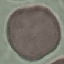
Result: no malaria parasites detected. Giemsa-stained preparation. Photographed with a smartphone camera at the microscope eyepiece. Automatically extracted cell patch, resized to 64 × 64 pixels. Thin blood film.